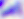
Summary:
  - Magnification: 400x
  - Modality: photomicrograph
  - Identification: Toxoplasma gondii